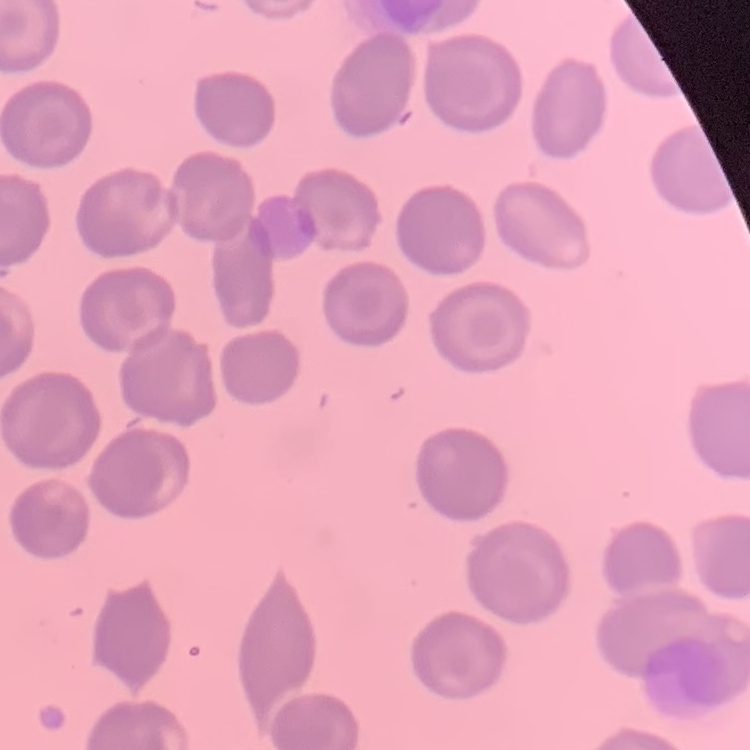

Summary:
  - Red blood cell morphology: no rouleaux formation
  - Preparation: thin blood film
  - Stain: Field's or Giemsa
  - Image type: one tile cut from a larger photomicrograph